Mark where platelets are.
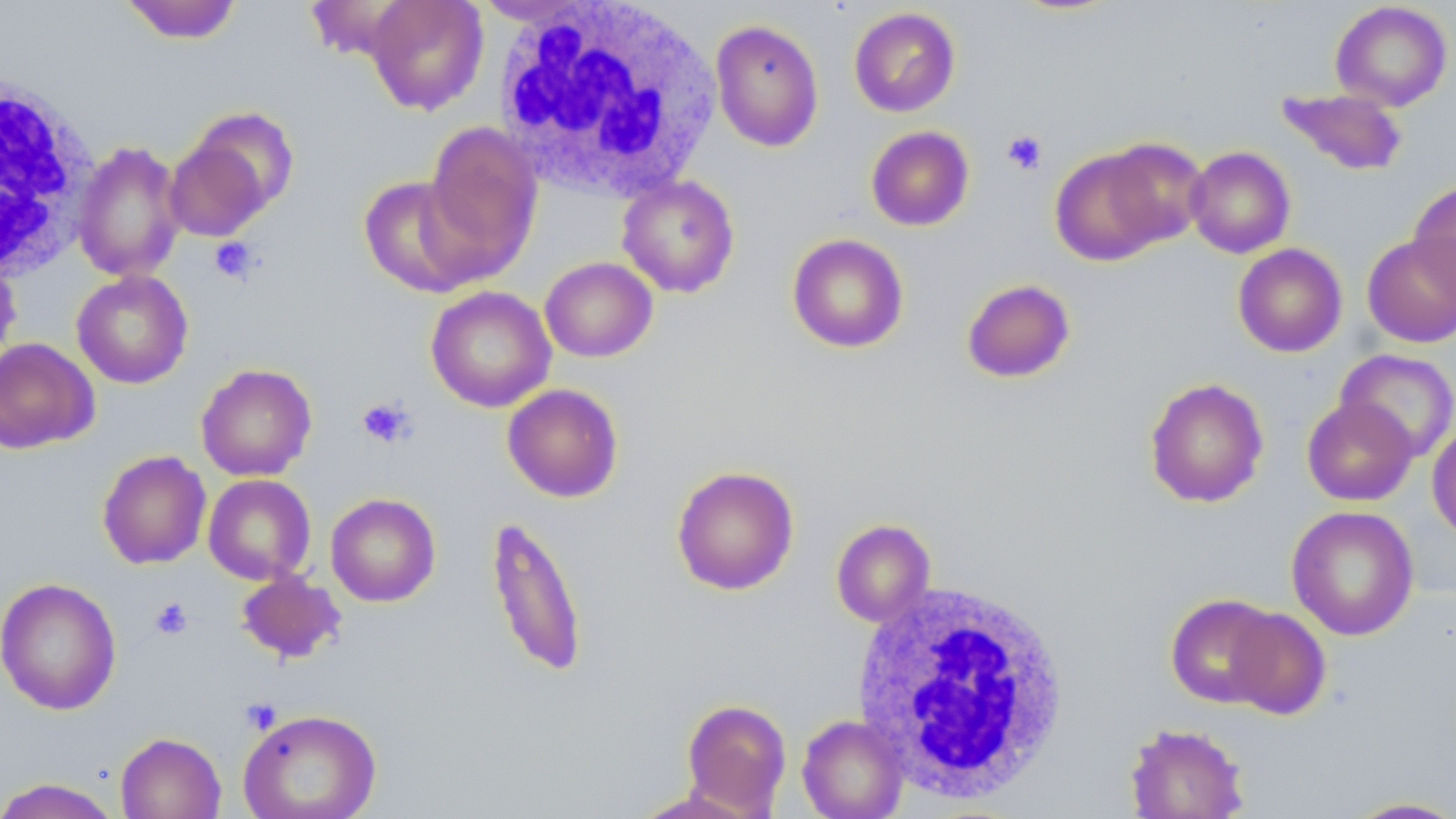

Approximate bounding boxes as (x1,y1)-(x2,y2) corner pairs in pixels.
Platelets: (1001,130)-(1047,176), (209,237)-(259,285), (355,396)-(416,449), (149,597)-(193,640), (240,697)-(282,734).

slide-level diagnosis = no evidence of blood parasites
modality = light microscopy
image size = 1456×819 pixels
field of view = single
magnification = 1000x
stain = May-Grünwald-Giemsa
uninfected red blood cell locations = approximate bounding boxes as (x1,y1)-(x2,y2) corner pairs in pixels: (120,0)-(244,44), (472,0)-(599,26), (364,1)-(489,115), (1330,1)-(1453,111), (848,6)-(961,117), (710,19)-(824,152), (1275,87)-(1409,177), (180,105)-(301,227), (423,121)-(543,270), (865,125)-(975,231), (1098,138)-(1209,249), (73,141)-(186,282), (1185,146)-(1295,258), (1049,147)-(1173,266), (617,175)-(741,298), (358,176)-(487,299), (1408,179)-(1456,300), (1362,232)-(1456,348), (786,233)-(909,353), (1233,243)-(1347,357), (540,256)-(658,362), (0,257)-(22,367), (71,270)-(194,388), (961,278)-(1076,383), (425,286)-(556,413), (0,337)-(99,454), (1335,348)-(1456,463), (195,363)-(317,481), (1144,377)-(1269,508), (502,383)-(624,503), (1302,397)-(1417,506), (1427,419)-(1456,542), (97,450)-(211,569), (671,465)-(800,596), (203,475)-(316,584), (325,492)-(441,607), (1286,505)-(1420,641), (484,514)-(588,679), (830,519)-(936,627), (236,572)-(346,665), (0,577)-(122,716), (1165,593)-(1282,708), (1224,606)-(1331,720), (680,698)-(792,816), (238,708)-(382,819), (797,714)-(909,819), (1124,722)-(1250,818), (115,732)-(227,819), (0,777)-(122,819), (628,788)-(767,819), (1340,796)-(1456,818)
white blood cell locations = approximate bounding boxes as (x1,y1)-(x2,y2) corner pairs in pixels: (494,0)-(721,200), (1,70)-(99,279), (852,579)-(1071,801)
preparation = thin blood smear